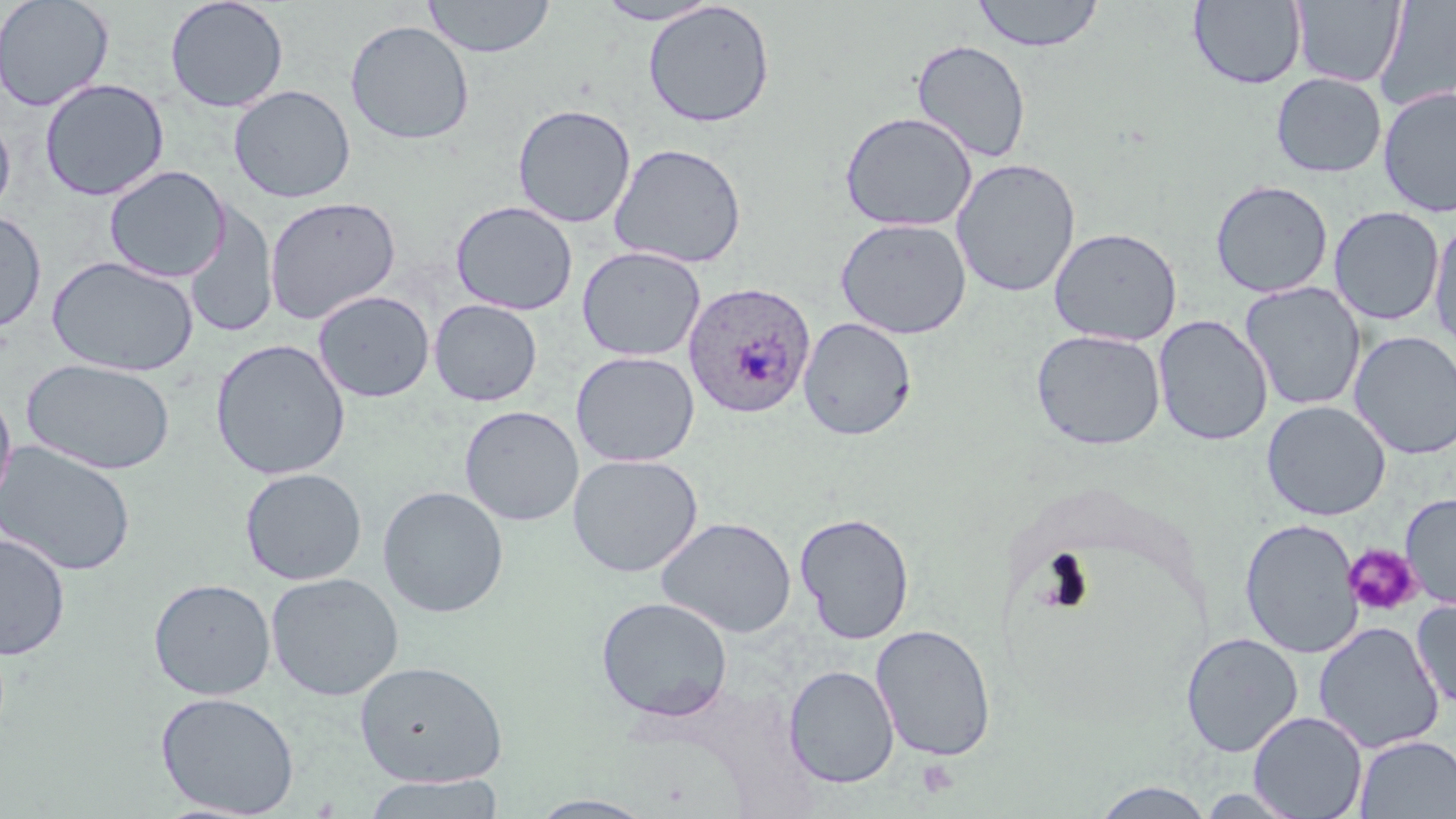

Plasmodium ovale-infected red blood cell locations = approximate bounding boxes as (x1,y1)-(x2,y2) corner pairs in pixels: (683,281)-(816,419)
slide-level diagnosis = Plasmodium ovale
modality = optical microscopy
field of view = one of a larger specimen
platelet locations = approximate bounding boxes as (x1,y1)-(x2,y2) corner pairs in pixels: (1343,543)-(1422,617), (916,758)-(960,799)
preparation = thin blood film
uninfected red blood cell locations = approximate bounding boxes as (x1,y1)-(x2,y2) corner pairs in pixels: (0,0)-(115,111), (164,0)-(289,113), (423,0)-(555,59), (593,0)-(723,25), (972,0)-(1104,53), (1291,0)-(1406,87), (1374,0)-(1455,113), (641,1)-(775,129), (1188,1)-(1307,89), (345,20)-(475,145), (911,39)-(1032,164), (1270,72)-(1386,178), (39,78)-(170,200), (228,84)-(356,203), (1377,86)-(1456,218), (512,104)-(636,228), (0,111)-(16,222), (840,111)-(977,232), (608,143)-(747,268), (951,158)-(1081,298), (104,165)-(229,282), (1210,180)-(1333,298), (264,195)-(401,325), (450,200)-(578,315), (183,205)-(278,340), (1329,206)-(1444,326), (0,211)-(46,334), (1428,217)-(1456,353), (836,218)-(972,339), (1048,227)-(1182,346), (577,246)-(705,361), (47,255)-(198,377), (1240,281)-(1366,411), (313,290)-(435,402), (429,299)-(543,406), (1153,315)-(1273,446), (798,317)-(917,440), (1031,329)-(1166,450), (1349,331)-(1456,460), (210,339)-(350,480), (571,351)-(700,467), (22,357)-(176,475), (0,385)-(17,512), (1261,400)-(1391,520), (459,405)-(583,526), (0,440)-(136,577), (567,453)-(703,577), (240,467)-(367,585), (377,486)-(509,618), (1400,492)-(1456,610), (794,511)-(915,644), (655,516)-(797,638), (1240,518)-(1364,658), (0,533)-(70,660), (266,572)-(404,701), (149,577)-(276,700), (596,595)-(733,721), (1411,597)-(1456,709), (1314,621)-(1445,754), (872,624)-(996,761), (1180,632)-(1304,757), (354,659)-(508,786), (784,665)-(899,788), (155,691)-(300,817), (1248,711)-(1368,819), (1353,735)-(1455,818), (360,774)-(507,819), (1091,781)-(1218,817), (528,795)-(656,818)
stain = May-Grünwald-Giemsa
image size = 1456×819 pixels
magnification = 1000x